Assess this cell for malaria.
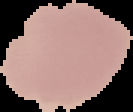

Uninfected.

Summary:
  - Image type: segmented cell region on a black background
  - Preparation: thin blood smear
  - Image size: 133×112 pixels